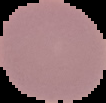
Summary:
  - Image size: 106×103 pixels
  - Malaria status: uninfected
  - Preparation: thin blood film
  - Image type: segmented cell region on a black background